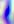

identification = Toxoplasma gondii
magnification = 400x
modality = micrograph